Classify this cell by malaria status.
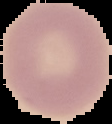

It is uninfected.

image size = 112×124 pixels
preparation = thin blood smear
image type = cell region segmented out of the field of view; surrounding area masked to black